Identify the parasite.
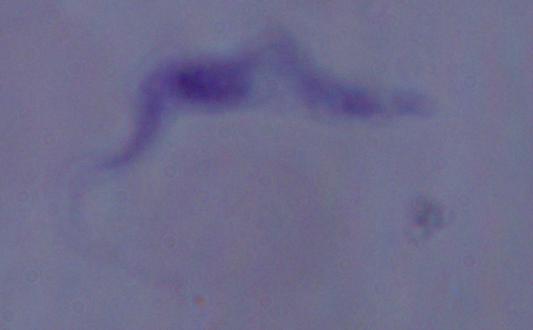
A trypanosome.

Micrograph. 1000x magnification.